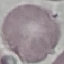
Result: negative for malaria parasites. Cell patch, automatically extracted from a larger field of view and resized to 64 × 64 pixels. Photographed with a smartphone camera at the microscope eyepiece. Giemsa-stained preparation. Thin blood film.